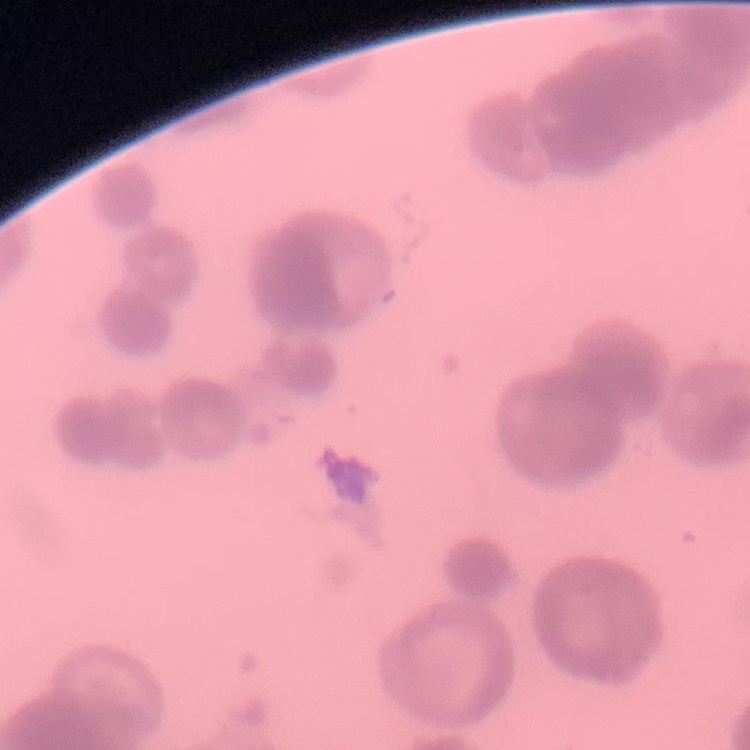
erythrocyte morphology = rouleaux formation
image type = one tile cut from a larger photomicrograph
preparation = thin blood film
stain = Field's or Giemsa